Assess this cell for malaria.
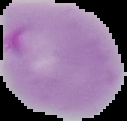
It is parasitized.

Summary:
  - Image type: segmented cell region on a black background
  - Preparation: thin blood smear
  - Image size: 127×121 pixels